Give the extent of all Plasmodium vivax-infected red blood cells.
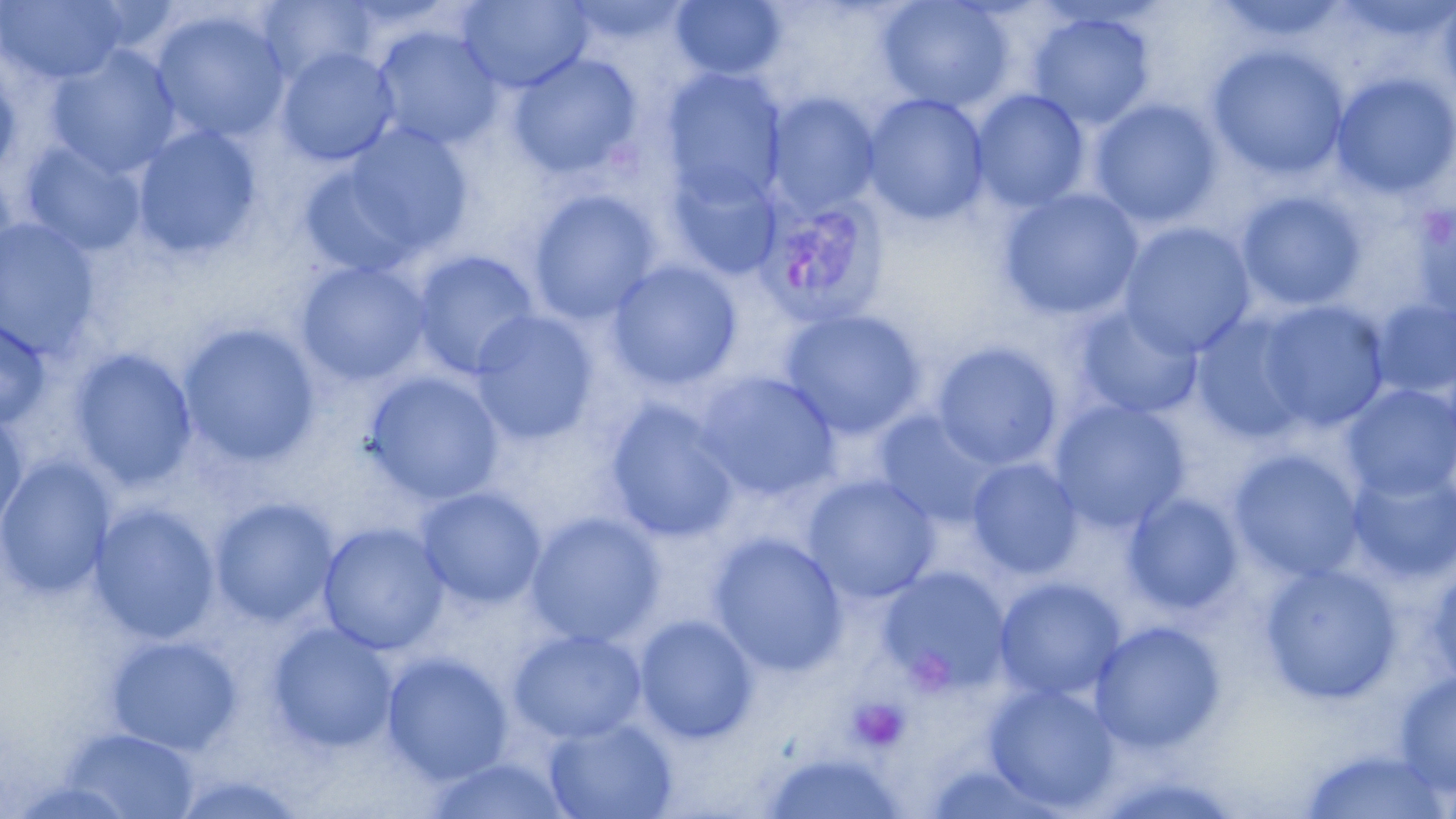

Approximate bounding boxes as named x1/y1/x2/y2 corners in pixels.
Plasmodium vivax-infected red blood cells: (x1=755, y1=191, x2=891, y2=328).

Uninfected red blood cell locations: (x1=1, y1=0, x2=130, y2=86), (x1=258, y1=0, x2=376, y2=86), (x1=458, y1=0, x2=592, y2=93), (x1=672, y1=0, x2=785, y2=80), (x1=876, y1=0, x2=1013, y2=113), (x1=1437, y1=0, x2=1456, y2=108), (x1=1215, y1=2, x2=1348, y2=44), (x1=149, y1=9, x2=291, y2=144), (x1=1029, y1=12, x2=1154, y2=129), (x1=371, y1=25, x2=503, y2=151), (x1=1207, y1=43, x2=1350, y2=181), (x1=47, y1=45, x2=181, y2=178), (x1=277, y1=47, x2=399, y2=166), (x1=508, y1=53, x2=643, y2=180), (x1=0, y1=54, x2=22, y2=180), (x1=660, y1=70, x2=787, y2=208), (x1=1331, y1=73, x2=1456, y2=199), (x1=970, y1=90, x2=1089, y2=212), (x1=766, y1=93, x2=880, y2=215), (x1=862, y1=93, x2=989, y2=225), (x1=1090, y1=99, x2=1223, y2=228), (x1=307, y1=125, x2=474, y2=276), (x1=132, y1=126, x2=262, y2=261), (x1=22, y1=142, x2=146, y2=257), (x1=668, y1=166, x2=782, y2=279), (x1=0, y1=172, x2=20, y2=288), (x1=999, y1=188, x2=1143, y2=321), (x1=528, y1=189, x2=661, y2=325), (x1=1236, y1=191, x2=1367, y2=312), (x1=1412, y1=204, x2=1456, y2=327), (x1=1, y1=218, x2=101, y2=359), (x1=1118, y1=222, x2=1255, y2=359), (x1=412, y1=250, x2=540, y2=380), (x1=295, y1=260, x2=431, y2=386), (x1=606, y1=260, x2=742, y2=391), (x1=1371, y1=298, x2=1456, y2=401), (x1=1256, y1=300, x2=1389, y2=432), (x1=1074, y1=304, x2=1203, y2=420), (x1=779, y1=309, x2=926, y2=439), (x1=469, y1=311, x2=600, y2=445), (x1=1192, y1=312, x2=1313, y2=442), (x1=0, y1=318, x2=51, y2=430), (x1=178, y1=323, x2=321, y2=467), (x1=932, y1=341, x2=1063, y2=470), (x1=70, y1=348, x2=197, y2=490), (x1=363, y1=371, x2=505, y2=505), (x1=695, y1=372, x2=840, y2=502), (x1=1342, y1=383, x2=1456, y2=503), (x1=604, y1=400, x2=741, y2=543), (x1=1049, y1=400, x2=1191, y2=534), (x1=0, y1=410, x2=29, y2=537), (x1=875, y1=411, x2=1000, y2=527), (x1=1229, y1=449, x2=1365, y2=582), (x1=0, y1=458, x2=116, y2=598), (x1=966, y1=458, x2=1083, y2=579), (x1=1347, y1=466, x2=1456, y2=585), (x1=802, y1=475, x2=940, y2=604), (x1=416, y1=486, x2=546, y2=609), (x1=1124, y1=493, x2=1243, y2=615), (x1=210, y1=497, x2=338, y2=626), (x1=89, y1=504, x2=220, y2=644), (x1=525, y1=512, x2=665, y2=648), (x1=318, y1=523, x2=449, y2=655), (x1=709, y1=533, x2=847, y2=677), (x1=1426, y1=561, x2=1456, y2=689), (x1=1259, y1=563, x2=1401, y2=705), (x1=877, y1=566, x2=1011, y2=696), (x1=993, y1=577, x2=1126, y2=702), (x1=633, y1=614, x2=759, y2=744), (x1=1089, y1=620, x2=1227, y2=754), (x1=267, y1=623, x2=398, y2=754), (x1=508, y1=629, x2=647, y2=745), (x1=105, y1=635, x2=242, y2=755), (x1=381, y1=652, x2=514, y2=786), (x1=1393, y1=670, x2=1456, y2=796), (x1=984, y1=682, x2=1120, y2=814), (x1=544, y1=716, x2=678, y2=819), (x1=62, y1=727, x2=200, y2=818), (x1=1296, y1=747, x2=1452, y2=819), (x1=756, y1=749, x2=909, y2=819), (x1=422, y1=754, x2=576, y2=819), (x1=917, y1=762, x2=1070, y2=819), (x1=166, y1=770, x2=312, y2=818). Platelet locations: (x1=847, y1=697, x2=912, y2=754). Slide-level diagnosis: Plasmodium vivax. One field of a larger specimen. Thin blood film. Captured at 1000x magnification. Light microscopy. May-Grünwald-Giemsa-stained preparation. Image is 1456×819 pixels.